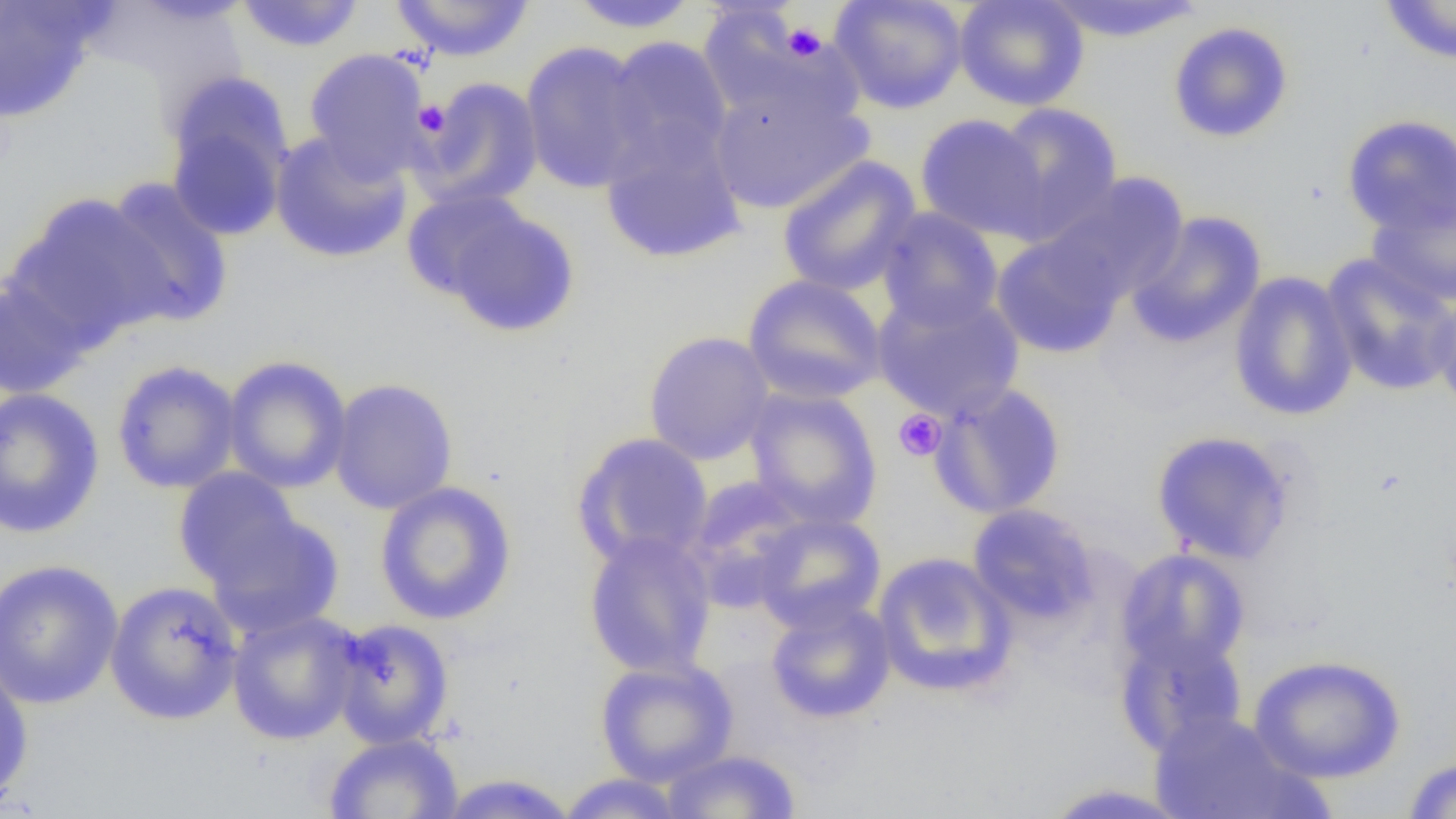 Approximate bounding boxes as [x1, y1, x2, y2] in pixels. Uninfected red blood cell locations: [565, 0, 702, 33], [830, 0, 968, 113], [953, 0, 1090, 111], [1042, 0, 1206, 43], [1378, 0, 1456, 64], [233, 1, 366, 53], [389, 1, 536, 62], [0, 2, 105, 122], [703, 14, 861, 138], [1168, 21, 1294, 143], [603, 36, 734, 173], [519, 41, 655, 194], [303, 48, 433, 180], [413, 77, 544, 211], [708, 83, 872, 215], [165, 84, 293, 240], [989, 102, 1124, 242], [914, 113, 1050, 241], [1341, 114, 1456, 237], [600, 125, 747, 264], [269, 130, 413, 264], [776, 156, 922, 297], [1044, 172, 1190, 304], [96, 178, 234, 329], [401, 189, 530, 302], [5, 192, 170, 347], [1367, 196, 1456, 308], [444, 205, 580, 337], [875, 207, 1004, 332], [1125, 211, 1267, 348], [990, 231, 1127, 359], [1320, 253, 1456, 396], [1228, 271, 1358, 421], [742, 274, 887, 405], [0, 277, 91, 401], [873, 288, 1025, 423], [1432, 293, 1456, 415], [643, 330, 775, 465], [222, 355, 353, 493], [111, 359, 242, 494], [328, 378, 459, 515], [928, 382, 1067, 520], [0, 386, 105, 539], [743, 387, 884, 529], [1150, 430, 1297, 566], [572, 433, 714, 570], [172, 468, 304, 591], [682, 476, 816, 612], [374, 480, 518, 625], [967, 503, 1100, 627], [753, 511, 886, 633], [207, 512, 344, 639], [582, 531, 718, 679], [1116, 547, 1251, 674], [872, 552, 1017, 699], [0, 558, 124, 710], [104, 580, 244, 725], [765, 598, 896, 724], [225, 609, 362, 746], [329, 618, 456, 749], [1113, 626, 1248, 758], [1248, 653, 1407, 783], [594, 656, 739, 786], [0, 657, 34, 806], [1148, 711, 1316, 819], [323, 732, 464, 819], [660, 749, 802, 818], [1401, 755, 1456, 817], [435, 773, 580, 818], [555, 773, 690, 818], [1037, 782, 1195, 818]. Platelet locations: [782, 22, 827, 61], [414, 100, 450, 136], [893, 410, 946, 461]. Slide-level diagnosis: negative for blood parasites. Image is 1456×819 pixels. 1000x magnification. Thin blood film. Optical microscopy. Single field of view.